Give the extent of all uninfected red blood cells.
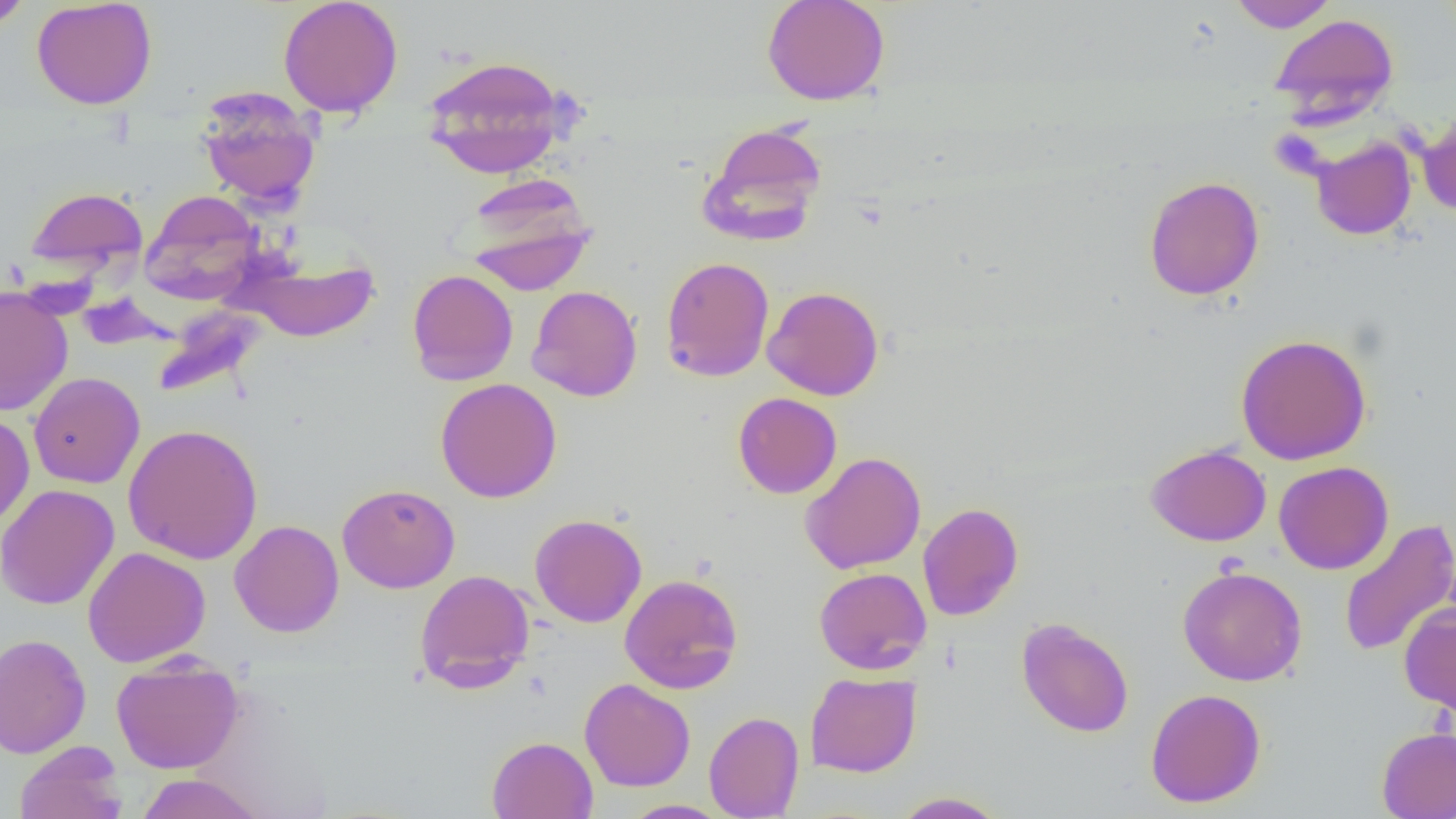
Approximate bounding boxes as named x1/y1/x2/y2 corners in pixels.
Uninfected red blood cells: (x1=0, y1=0, x2=33, y2=31), (x1=761, y1=0, x2=891, y2=105), (x1=1226, y1=0, x2=1338, y2=32), (x1=31, y1=1, x2=158, y2=109), (x1=277, y1=1, x2=404, y2=117), (x1=1269, y1=13, x2=1399, y2=124), (x1=420, y1=54, x2=573, y2=179), (x1=196, y1=89, x2=321, y2=209), (x1=1417, y1=111, x2=1456, y2=217), (x1=698, y1=121, x2=828, y2=246), (x1=1310, y1=137, x2=1416, y2=240), (x1=460, y1=174, x2=596, y2=294), (x1=1143, y1=176, x2=1264, y2=301), (x1=24, y1=185, x2=148, y2=276), (x1=140, y1=190, x2=264, y2=303), (x1=229, y1=252, x2=379, y2=342), (x1=660, y1=256, x2=775, y2=382), (x1=407, y1=269, x2=519, y2=386), (x1=526, y1=285, x2=642, y2=401), (x1=762, y1=285, x2=884, y2=400), (x1=0, y1=286, x2=73, y2=416), (x1=155, y1=305, x2=268, y2=397), (x1=1235, y1=333, x2=1372, y2=465), (x1=28, y1=372, x2=145, y2=489), (x1=435, y1=377, x2=562, y2=503), (x1=732, y1=392, x2=842, y2=499), (x1=0, y1=411, x2=34, y2=529), (x1=123, y1=423, x2=264, y2=565), (x1=1146, y1=444, x2=1272, y2=546), (x1=799, y1=451, x2=927, y2=574), (x1=1273, y1=461, x2=1393, y2=574), (x1=0, y1=483, x2=119, y2=611), (x1=337, y1=483, x2=460, y2=593), (x1=917, y1=502, x2=1023, y2=621), (x1=530, y1=513, x2=647, y2=628), (x1=1338, y1=518, x2=1456, y2=658), (x1=229, y1=520, x2=344, y2=637), (x1=83, y1=546, x2=211, y2=668), (x1=1177, y1=565, x2=1307, y2=686), (x1=814, y1=567, x2=932, y2=675), (x1=414, y1=569, x2=535, y2=692), (x1=619, y1=573, x2=744, y2=693), (x1=1398, y1=602, x2=1456, y2=716), (x1=1016, y1=617, x2=1134, y2=738), (x1=0, y1=633, x2=91, y2=758), (x1=111, y1=656, x2=244, y2=773), (x1=805, y1=671, x2=922, y2=778), (x1=579, y1=678, x2=695, y2=792), (x1=1145, y1=688, x2=1267, y2=808), (x1=704, y1=710, x2=804, y2=819), (x1=1377, y1=726, x2=1456, y2=819), (x1=487, y1=736, x2=598, y2=819), (x1=14, y1=741, x2=128, y2=819), (x1=134, y1=773, x2=266, y2=818), (x1=891, y1=791, x2=1009, y2=818), (x1=620, y1=800, x2=732, y2=819).

Summary:
  - Slide-level diagnosis: negative for blood parasites
  - Magnification: 1000x
  - Modality: optical microscopy
  - Preparation: thin blood film
  - Field of view: single
  - Image size: 1456×819 pixels